Assess this cell for malaria.
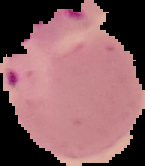
It is parasitized.

Summary:
  - Preparation: thin blood smear
  - Image type: cell region segmented out of the field of view; surrounding area masked to black
  - Image size: 145×166 pixels